Outline each blood parasite and name the species.
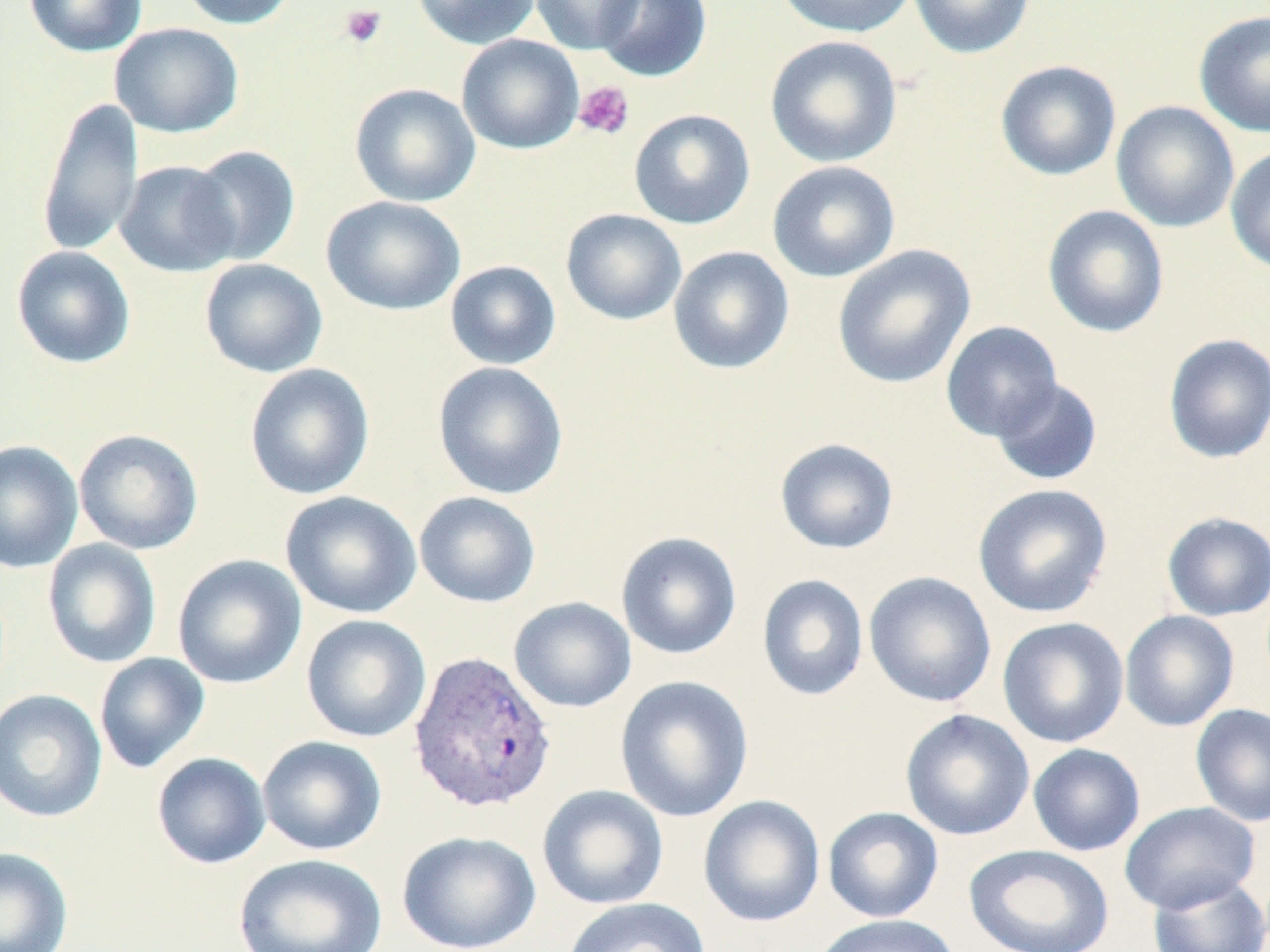
Approximate bounding boxes as (x1,y1)-(x2,y2) corner pairs in pixels.
Plasmodium vivax-infected red blood cells: (407,648)-(557,814).
No Plasmodium falciparum, Plasmodium ovale, Plasmodium malariae, Babesia divergens, or Trypanosoma brucei observed.

slide-level diagnosis = Plasmodium vivax
magnification = 1000x
platelet locations (subset) = approximate bounding boxes as (x1,y1)-(x2,y2) corner pairs in pixels: (339,4)-(387,48), (573,81)-(635,141)
modality = light microscopy
image size = 1270×952 pixels
field of view = single
stain = May-Grünwald-Giemsa
preparation = thin blood film
uninfected red blood cell locations (subset) = approximate bounding boxes as (x1,y1)-(x2,y2) corner pairs in pixels: (24,0)-(147,57), (177,0)-(299,30), (411,0)-(541,49), (530,0)-(645,55), (773,0)-(916,39), (908,0)-(1037,59), (1193,10)-(1270,138), (109,22)-(244,138), (456,34)-(585,155), (764,34)-(902,168), (995,60)-(1122,181), (349,82)-(481,207), (36,97)-(143,257), (1111,100)-(1240,233), (629,108)-(756,229), (1225,144)-(1270,276), (187,145)-(301,266), (115,160)-(240,277), (767,160)-(900,282), (321,196)-(466,316), (1042,204)-(1170,338), (561,208)-(687,326), (832,244)-(977,389), (11,245)-(136,369), (668,246)-(795,375), (199,258)-(328,378), (445,260)-(562,370), (940,321)-(1063,441), (1163,333)-(1270,464), (432,361)-(568,500), (244,362)-(375,501), (989,377)-(1104,486), (74,428)-(204,555), (774,438)-(899,555), (0,439)-(84,574), (973,483)-(1113,618), (280,491)-(422,619), (414,491)-(541,608), (1161,511)-(1270,621), (616,531)-(742,660), (42,539)-(162,669), (172,553)-(307,690), (863,571)-(997,708), (757,573)-(869,701), (509,596)-(636,713), (1119,610)-(1240,732), (300,614)-(432,744), (997,616)-(1129,748), (94,653)-(210,774), (615,674)-(754,823), (0,689)-(107,823), (1190,702)-(1270,827), (899,709)-(1035,841), (257,735)-(387,856), (1027,743)-(1145,856), (151,752)-(271,870), (537,784)-(669,911), (698,795)-(825,928), (1120,801)-(1260,914), (822,806)-(944,923), (397,830)-(541,952), (964,844)-(1115,952), (0,846)-(74,952), (233,853)-(388,952), (1148,871)-(1270,952), (562,897)-(711,952), (811,914)-(960,952)